Outline each Plasmodium ovale-infected red blood cell.
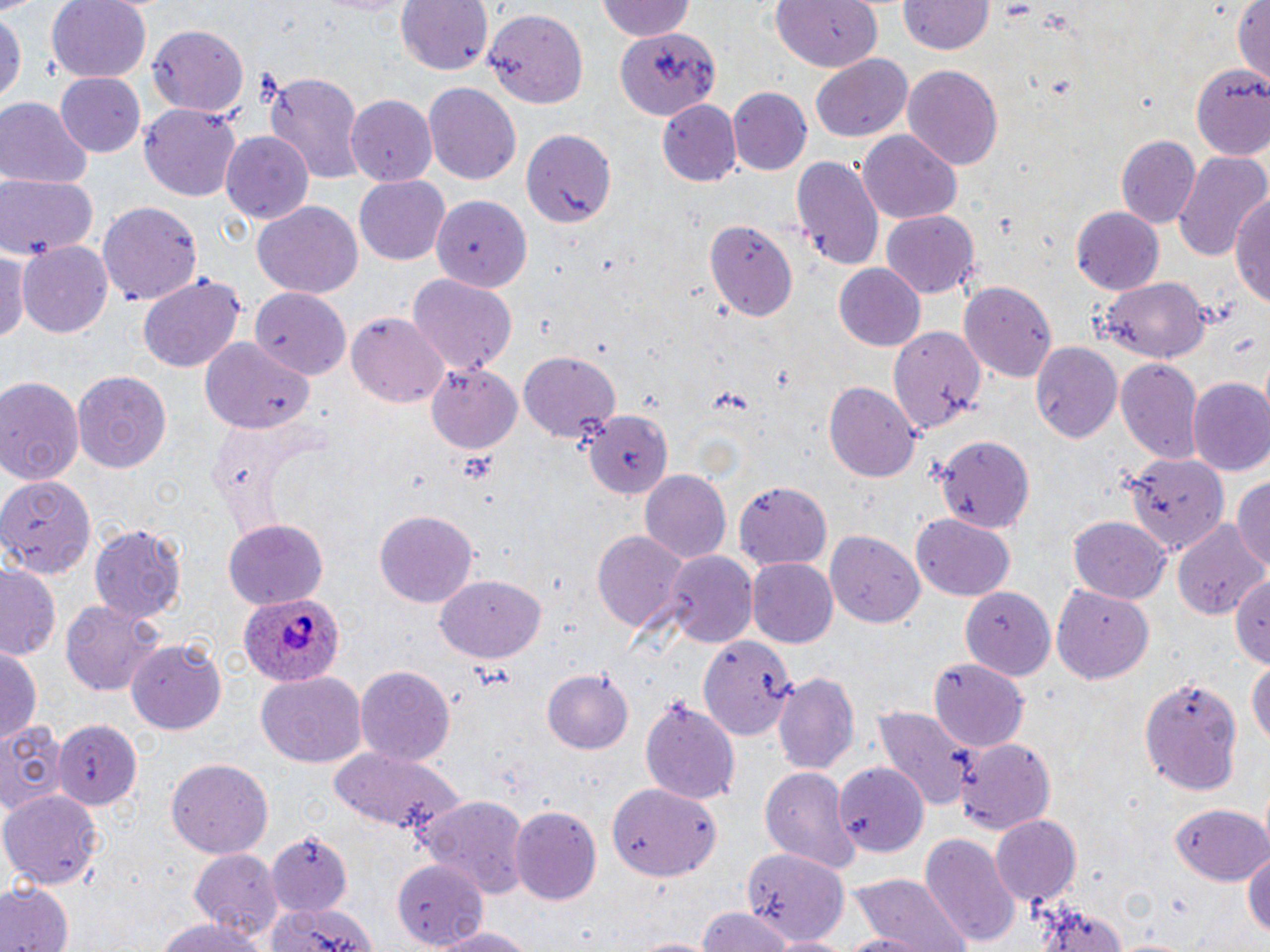

Approximate bounding boxes as named x1/y1/x2/y2 corners in pixels.
Plasmodium ovale-infected red blood cells: (x1=239, y1=596, x2=347, y2=690).

{
  "slide_level_diagnosis": "Plasmodium ovale",
  "stain": "May-Grünwald-Giemsa",
  "field_of_view": "one of a larger specimen",
  "modality": "optical microscopy",
  "preparation": "thin blood smear",
  "image_size": "1270×952 pixels",
  "magnification": "1000x",
  "uninfected_red_blood_cell_locations": "approximate bounding boxes as named x1/y1/x2/y2 corners in pixels: (x1=46, y1=0, x2=153, y2=84), (x1=394, y1=0, x2=493, y2=76), (x1=595, y1=0, x2=697, y2=43), (x1=769, y1=0, x2=882, y2=74), (x1=898, y1=0, x2=996, y2=55), (x1=1233, y1=0, x2=1269, y2=86), (x1=0, y1=8, x2=24, y2=113), (x1=482, y1=8, x2=589, y2=111), (x1=148, y1=25, x2=248, y2=118), (x1=616, y1=29, x2=719, y2=121), (x1=810, y1=53, x2=914, y2=143), (x1=1193, y1=64, x2=1268, y2=157), (x1=901, y1=65, x2=1005, y2=170), (x1=262, y1=70, x2=368, y2=186), (x1=56, y1=75, x2=147, y2=159), (x1=424, y1=82, x2=522, y2=185), (x1=728, y1=87, x2=812, y2=174), (x1=344, y1=94, x2=437, y2=184), (x1=0, y1=98, x2=91, y2=186), (x1=658, y1=99, x2=742, y2=186), (x1=141, y1=103, x2=244, y2=201), (x1=520, y1=127, x2=617, y2=228), (x1=860, y1=129, x2=962, y2=221), (x1=220, y1=131, x2=314, y2=223), (x1=1118, y1=135, x2=1199, y2=230), (x1=1170, y1=149, x2=1267, y2=261), (x1=791, y1=152, x2=885, y2=271), (x1=0, y1=174, x2=100, y2=261), (x1=354, y1=176, x2=450, y2=266), (x1=1231, y1=188, x2=1270, y2=313), (x1=433, y1=194, x2=531, y2=291), (x1=252, y1=201, x2=363, y2=298), (x1=98, y1=202, x2=202, y2=304), (x1=1071, y1=206, x2=1164, y2=295), (x1=882, y1=210, x2=979, y2=297), (x1=706, y1=221, x2=798, y2=323), (x1=18, y1=240, x2=114, y2=337), (x1=0, y1=244, x2=26, y2=350), (x1=834, y1=265, x2=924, y2=352), (x1=137, y1=273, x2=246, y2=372), (x1=408, y1=274, x2=516, y2=374), (x1=1098, y1=276, x2=1210, y2=363), (x1=960, y1=279, x2=1055, y2=381), (x1=247, y1=286, x2=352, y2=373), (x1=346, y1=312, x2=450, y2=408), (x1=884, y1=325, x2=986, y2=434), (x1=201, y1=337, x2=309, y2=434), (x1=1029, y1=340, x2=1123, y2=442), (x1=519, y1=353, x2=620, y2=443), (x1=1115, y1=359, x2=1202, y2=465), (x1=424, y1=363, x2=523, y2=454), (x1=73, y1=370, x2=172, y2=477), (x1=0, y1=375, x2=85, y2=484), (x1=1187, y1=377, x2=1270, y2=476), (x1=824, y1=382, x2=921, y2=481), (x1=582, y1=409, x2=672, y2=502), (x1=935, y1=434, x2=1035, y2=535), (x1=1122, y1=449, x2=1231, y2=553), (x1=641, y1=468, x2=731, y2=563), (x1=0, y1=472, x2=96, y2=577), (x1=1231, y1=477, x2=1270, y2=576), (x1=733, y1=482, x2=833, y2=571), (x1=375, y1=509, x2=477, y2=608), (x1=910, y1=514, x2=1015, y2=600), (x1=1068, y1=516, x2=1170, y2=602), (x1=222, y1=520, x2=328, y2=608), (x1=1174, y1=520, x2=1267, y2=622), (x1=89, y1=523, x2=186, y2=621), (x1=592, y1=529, x2=690, y2=636), (x1=825, y1=530, x2=924, y2=628), (x1=658, y1=550, x2=755, y2=648), (x1=748, y1=558, x2=840, y2=649), (x1=1, y1=560, x2=62, y2=660), (x1=1232, y1=570, x2=1270, y2=670), (x1=434, y1=574, x2=542, y2=660), (x1=1052, y1=582, x2=1154, y2=681), (x1=961, y1=587, x2=1055, y2=680), (x1=61, y1=601, x2=162, y2=695), (x1=699, y1=634, x2=796, y2=740), (x1=129, y1=639, x2=227, y2=735), (x1=0, y1=644, x2=41, y2=745), (x1=928, y1=657, x2=1028, y2=750), (x1=1247, y1=658, x2=1270, y2=753), (x1=355, y1=664, x2=456, y2=765), (x1=542, y1=670, x2=633, y2=754), (x1=255, y1=671, x2=366, y2=768), (x1=773, y1=671, x2=861, y2=779), (x1=1137, y1=674, x2=1245, y2=799), (x1=640, y1=696, x2=743, y2=806), (x1=869, y1=702, x2=975, y2=813), (x1=55, y1=717, x2=142, y2=809), (x1=0, y1=720, x2=68, y2=820), (x1=953, y1=737, x2=1057, y2=835), (x1=327, y1=747, x2=465, y2=839), (x1=165, y1=757, x2=273, y2=859), (x1=834, y1=762, x2=927, y2=856), (x1=759, y1=766, x2=862, y2=871), (x1=609, y1=784, x2=720, y2=882), (x1=1, y1=789, x2=102, y2=889), (x1=416, y1=793, x2=530, y2=900), (x1=1173, y1=802, x2=1268, y2=887), (x1=508, y1=804, x2=602, y2=904), (x1=992, y1=813, x2=1083, y2=905), (x1=263, y1=824, x2=358, y2=916), (x1=919, y1=832, x2=1022, y2=950), (x1=1244, y1=845, x2=1270, y2=943), (x1=743, y1=847, x2=851, y2=945), (x1=187, y1=848, x2=282, y2=941), (x1=393, y1=858, x2=494, y2=943), (x1=851, y1=874, x2=968, y2=952), (x1=1, y1=882, x2=73, y2=952), (x1=1028, y1=894, x2=1131, y2=952), (x1=267, y1=897, x2=379, y2=952), (x1=694, y1=910, x2=801, y2=952), (x1=153, y1=917, x2=263, y2=952), (x1=426, y1=924, x2=541, y2=951), (x1=828, y1=932, x2=943, y2=952)"
}